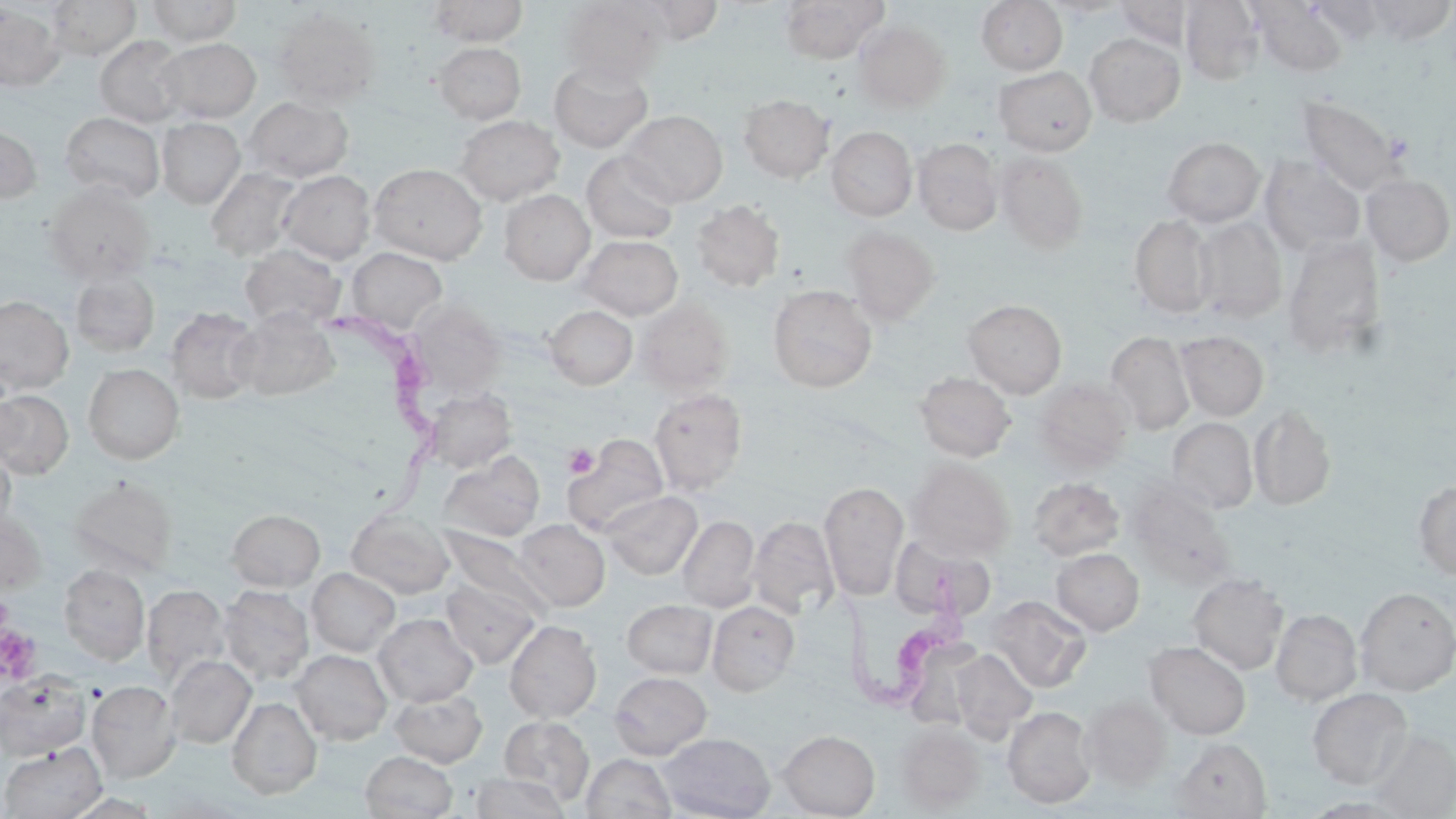

Approximate bounding boxes as (x1, y1, x2, y2) in pixels. Trypanosoma brucei locations: (330, 312, 444, 525), (834, 570, 964, 719). Uninfected red blood cell locations: (47, 0, 141, 60), (427, 0, 528, 46), (559, 0, 667, 84), (779, 0, 889, 63), (976, 0, 1068, 75), (1043, 0, 1130, 19), (1180, 0, 1263, 85), (1366, 0, 1455, 44), (145, 1, 242, 46), (621, 1, 730, 44), (1113, 1, 1195, 48), (1252, 1, 1348, 77), (0, 5, 64, 91), (271, 7, 381, 108), (853, 21, 950, 111), (1084, 33, 1185, 126), (95, 35, 189, 126), (158, 38, 261, 123), (433, 42, 526, 124), (549, 58, 654, 152), (994, 66, 1097, 155), (739, 94, 834, 182), (1296, 95, 1407, 196), (244, 96, 354, 182), (622, 110, 727, 206), (60, 111, 165, 203), (455, 115, 564, 205), (157, 118, 245, 209), (0, 123, 41, 203), (826, 126, 917, 221), (1163, 137, 1265, 227), (914, 138, 1003, 235), (581, 151, 680, 244), (996, 151, 1089, 253), (1259, 156, 1366, 255), (369, 163, 488, 264), (206, 168, 301, 261), (279, 170, 375, 263), (1362, 173, 1455, 266), (45, 183, 156, 284), (500, 190, 595, 284), (691, 199, 784, 291), (1129, 214, 1215, 318), (1193, 216, 1287, 323), (842, 226, 940, 323), (578, 235, 682, 319), (1283, 235, 1386, 361), (240, 244, 346, 331), (348, 247, 447, 333), (71, 270, 159, 356), (768, 285, 877, 392), (1, 295, 73, 394), (635, 298, 734, 395), (410, 299, 504, 394), (963, 299, 1067, 398), (544, 304, 638, 390), (166, 307, 262, 403), (232, 311, 339, 401), (1107, 331, 1195, 434), (1177, 331, 1269, 421), (83, 364, 184, 464), (914, 372, 1016, 462), (1032, 378, 1134, 471), (422, 388, 516, 472), (649, 388, 748, 495), (0, 390, 73, 478), (1249, 403, 1336, 511), (1168, 418, 1258, 513), (567, 436, 667, 536), (0, 445, 15, 532), (439, 451, 545, 541), (907, 458, 1015, 560), (68, 475, 178, 576), (1028, 477, 1125, 560), (819, 480, 908, 599), (1413, 480, 1456, 580), (1126, 486, 1237, 588), (604, 491, 702, 579), (346, 507, 455, 600), (0, 509, 46, 594), (227, 509, 325, 591), (678, 515, 760, 612), (748, 515, 838, 618), (513, 519, 609, 610), (440, 529, 550, 620), (892, 539, 999, 623), (1051, 548, 1144, 634), (58, 564, 149, 665), (307, 568, 401, 656), (1188, 573, 1289, 674), (440, 576, 541, 667), (143, 584, 230, 685), (219, 585, 314, 684), (1355, 587, 1456, 694), (989, 595, 1092, 692), (622, 599, 717, 678), (707, 601, 800, 695), (1271, 609, 1362, 705), (374, 614, 478, 706), (504, 620, 601, 723), (1145, 641, 1251, 739), (950, 648, 1036, 740), (292, 649, 392, 744), (165, 655, 256, 748), (609, 671, 712, 759), (0, 673, 91, 760), (87, 680, 181, 782), (1307, 688, 1413, 789), (390, 689, 488, 767), (227, 696, 322, 799), (1080, 696, 1171, 789), (1002, 706, 1097, 808), (499, 715, 594, 805), (896, 722, 985, 812), (778, 729, 879, 818), (1366, 729, 1456, 819), (658, 733, 776, 818), (1173, 737, 1271, 818), (1, 743, 107, 819), (360, 751, 457, 819), (581, 753, 676, 819), (468, 773, 572, 819). Platelet locations: (564, 443, 598, 478), (0, 624, 41, 684). Slide-level diagnosis: Trypanosoma brucei. May-Grünwald-Giemsa-stained preparation. One field of a larger specimen. Captured at 1000x magnification. Image is 1456×819 pixels. Thin blood smear. Optical microscopy.